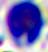

Summary:
  - Magnification: 400x
  - Modality: micrograph
  - Identification: leukocyte